Classify this cell by malaria status.
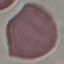

It is uninfected.

stain = Giemsa
capture = smartphone through the microscope eyepiece
image type = cell patch, automatically extracted from a larger field of view and resized to 64 × 64 pixels
preparation = thin blood smear